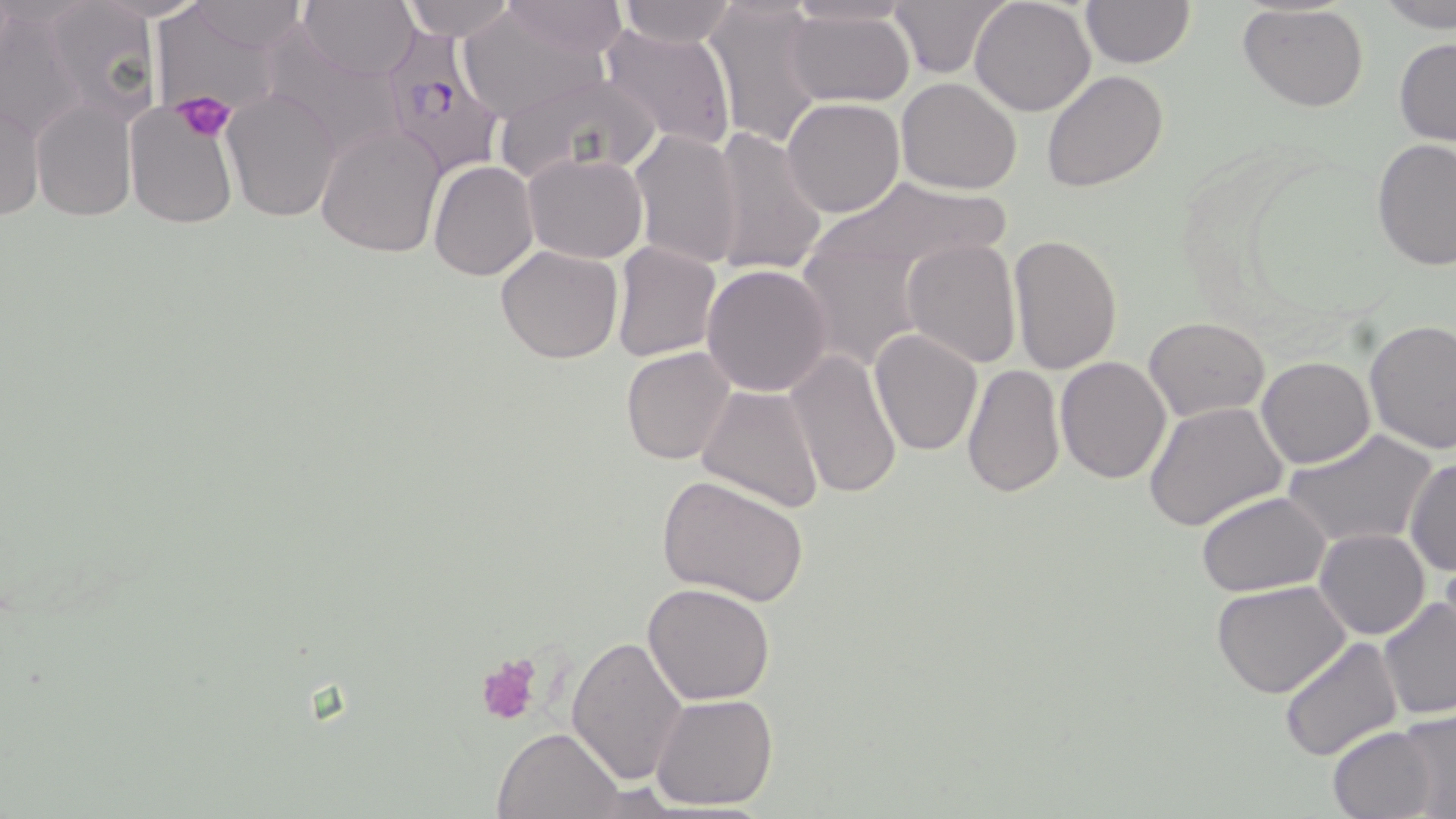
Summary:
  - Coordinate format: approximate bounding boxes as named x1/y1/x2/y2 corners in pixels
  - Platelet locations: (x1=173, y1=89, x2=238, y2=142), (x1=477, y1=654, x2=542, y2=726)
  - Uninfected red blood cell locations: (x1=297, y1=0, x2=419, y2=82), (x1=403, y1=0, x2=516, y2=41), (x1=783, y1=0, x2=916, y2=32), (x1=888, y1=0, x2=1011, y2=80), (x1=970, y1=0, x2=1096, y2=116), (x1=496, y1=1, x2=628, y2=61), (x1=614, y1=1, x2=737, y2=48), (x1=704, y1=1, x2=828, y2=147), (x1=1080, y1=1, x2=1196, y2=69), (x1=1377, y1=1, x2=1456, y2=31), (x1=36, y1=2, x2=161, y2=126), (x1=183, y1=2, x2=313, y2=52), (x1=1238, y1=4, x2=1369, y2=112), (x1=0, y1=6, x2=92, y2=144), (x1=456, y1=7, x2=611, y2=121), (x1=784, y1=8, x2=915, y2=108), (x1=258, y1=27, x2=407, y2=165), (x1=598, y1=27, x2=738, y2=147), (x1=931, y1=28, x2=1086, y2=165), (x1=1393, y1=37, x2=1456, y2=147), (x1=493, y1=67, x2=663, y2=185), (x1=1041, y1=69, x2=1168, y2=192), (x1=896, y1=78, x2=1021, y2=194), (x1=222, y1=87, x2=342, y2=223), (x1=1, y1=93, x2=43, y2=224), (x1=783, y1=98, x2=905, y2=219), (x1=31, y1=100, x2=137, y2=222), (x1=123, y1=101, x2=239, y2=229), (x1=316, y1=123, x2=445, y2=258), (x1=707, y1=125, x2=828, y2=278), (x1=629, y1=128, x2=745, y2=271), (x1=1372, y1=138, x2=1455, y2=270), (x1=523, y1=153, x2=647, y2=263), (x1=428, y1=161, x2=538, y2=280), (x1=826, y1=177, x2=1013, y2=283), (x1=1007, y1=235, x2=1124, y2=376), (x1=902, y1=238, x2=1021, y2=367), (x1=609, y1=241, x2=722, y2=363), (x1=495, y1=246, x2=623, y2=366), (x1=889, y1=251, x2=1021, y2=482), (x1=701, y1=263, x2=834, y2=398), (x1=1144, y1=317, x2=1271, y2=421), (x1=1363, y1=319, x2=1456, y2=453), (x1=869, y1=329, x2=984, y2=456), (x1=620, y1=348, x2=736, y2=466), (x1=784, y1=348, x2=904, y2=502), (x1=1055, y1=356, x2=1173, y2=483), (x1=1258, y1=357, x2=1375, y2=469), (x1=960, y1=364, x2=1065, y2=501), (x1=695, y1=384, x2=824, y2=514), (x1=1142, y1=401, x2=1288, y2=531), (x1=1283, y1=429, x2=1440, y2=551), (x1=1403, y1=455, x2=1456, y2=576), (x1=658, y1=473, x2=810, y2=609), (x1=1194, y1=491, x2=1332, y2=597), (x1=1314, y1=529, x2=1431, y2=640), (x1=643, y1=581, x2=776, y2=703), (x1=1212, y1=582, x2=1352, y2=698), (x1=1377, y1=595, x2=1455, y2=721), (x1=566, y1=635, x2=688, y2=785), (x1=1278, y1=635, x2=1404, y2=761), (x1=651, y1=693, x2=779, y2=812), (x1=1396, y1=710, x2=1456, y2=816), (x1=1327, y1=723, x2=1446, y2=819), (x1=491, y1=727, x2=625, y2=817)
  - Plasmodium falciparum-infected red blood cell locations: (x1=376, y1=21, x2=506, y2=180)
  - Slide-level diagnosis: Plasmodium falciparum
  - Stain: May-Grünwald-Giemsa
  - Magnification: 1000x
  - Image size: 1456×819 pixels
  - Modality: optical microscopy
  - Field of view: single
  - Preparation: thin blood film